Identify the parasite.
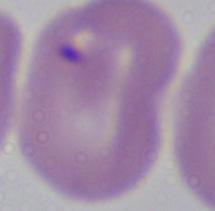

This is Babesia.

Summary:
  - Modality: photomicrograph
  - Magnification: 1000x